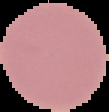
{
  "image_type": "segmented cell region on a black background",
  "preparation": "thin blood film",
  "image_size": "109×112 pixels",
  "result": "no Plasmodium parasites detected"
}